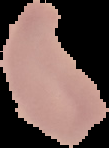 Image is 109×148 pixels. The area outside the segmented cell region is set to black. From a thin blood smear. Result: no malaria parasites seen.